Assess this cell for malaria.
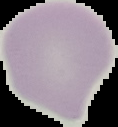
It is uninfected.

Image is 118×127 pixels. From a thin blood smear. Cell region segmented out of the field of view; the surrounding area is masked to black.